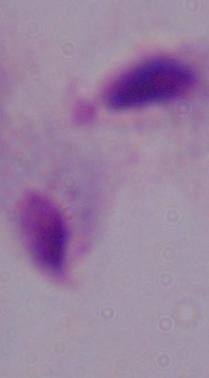
Summary:
  - Identification: trichomonad
  - Modality: micrograph
  - Magnification: 1000x